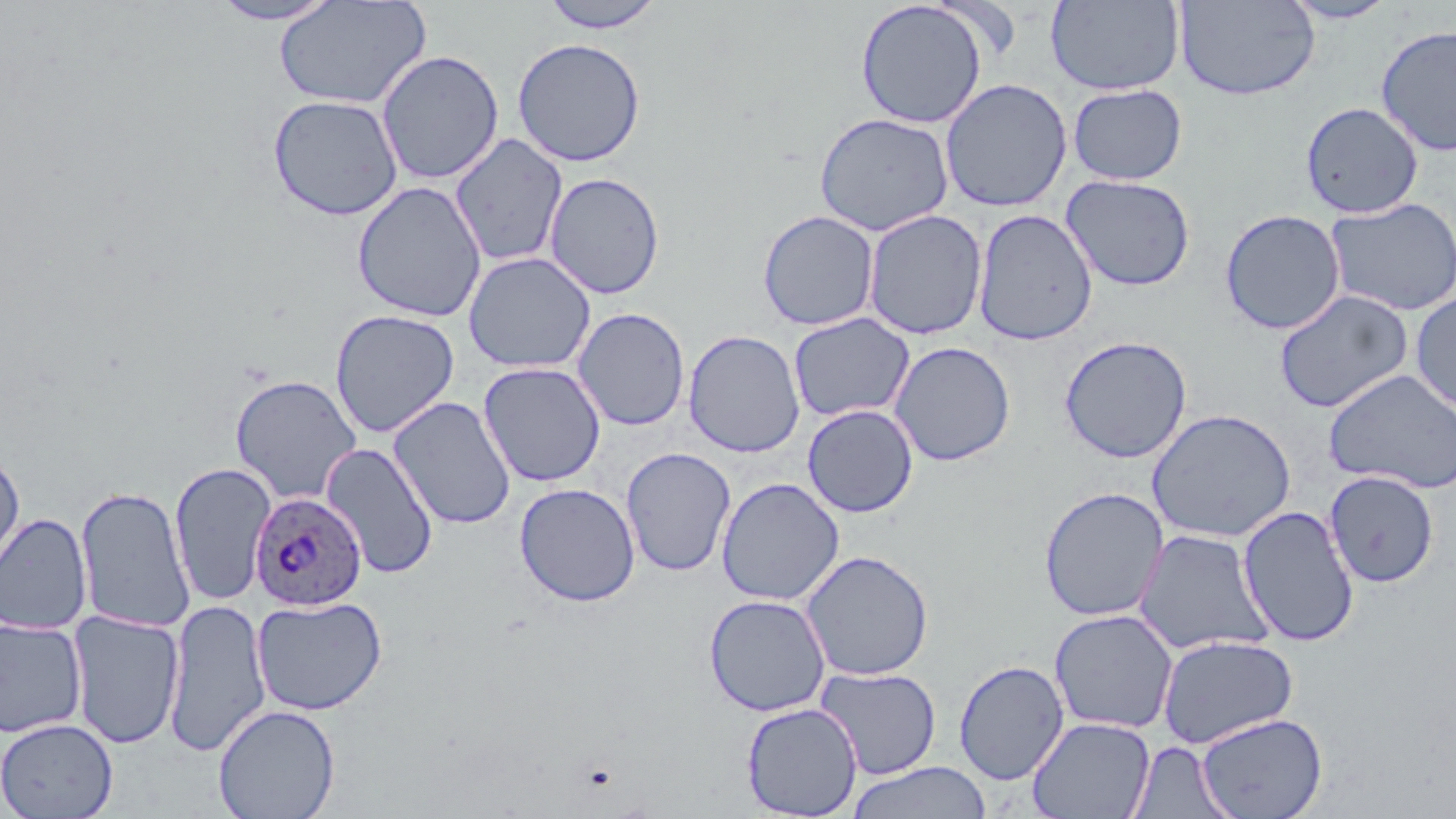
slide-level diagnosis = Plasmodium ovale
magnification = 1000x
Plasmodium ovale-infected red blood cell locations = approximate bounding boxes as named x1/y1/x2/y2 corners in pixels: (x1=249, y1=492, x2=366, y2=611)
modality = optical microscopy
field of view = one of a larger specimen
image size = 1456×819 pixels
uninfected red blood cell locations = approximate bounding boxes as named x1/y1/x2/y2 corners in pixels: (x1=207, y1=0, x2=343, y2=25), (x1=537, y1=0, x2=667, y2=33), (x1=1174, y1=0, x2=1320, y2=101), (x1=274, y1=1, x2=431, y2=110), (x1=855, y1=1, x2=988, y2=129), (x1=1046, y1=1, x2=1185, y2=95), (x1=1280, y1=1, x2=1399, y2=24), (x1=1375, y1=24, x2=1456, y2=158), (x1=511, y1=37, x2=646, y2=167), (x1=376, y1=49, x2=504, y2=185), (x1=939, y1=78, x2=1073, y2=212), (x1=1067, y1=84, x2=1188, y2=186), (x1=267, y1=94, x2=404, y2=221), (x1=1300, y1=101, x2=1423, y2=218), (x1=814, y1=112, x2=954, y2=236), (x1=449, y1=132, x2=568, y2=268), (x1=544, y1=171, x2=665, y2=300), (x1=1060, y1=174, x2=1196, y2=291), (x1=352, y1=181, x2=487, y2=322), (x1=1324, y1=197, x2=1456, y2=317), (x1=757, y1=209, x2=880, y2=331), (x1=862, y1=209, x2=988, y2=340), (x1=972, y1=209, x2=1098, y2=346), (x1=1220, y1=209, x2=1346, y2=335), (x1=463, y1=252, x2=596, y2=373), (x1=1274, y1=289, x2=1413, y2=413), (x1=1410, y1=292, x2=1456, y2=416), (x1=572, y1=307, x2=690, y2=431), (x1=329, y1=309, x2=460, y2=439), (x1=788, y1=312, x2=915, y2=423), (x1=683, y1=329, x2=805, y2=458), (x1=1058, y1=335, x2=1193, y2=464), (x1=889, y1=341, x2=1016, y2=466), (x1=478, y1=361, x2=606, y2=487), (x1=1324, y1=368, x2=1456, y2=494), (x1=230, y1=374, x2=362, y2=505), (x1=388, y1=395, x2=516, y2=530), (x1=802, y1=405, x2=918, y2=517), (x1=1146, y1=408, x2=1297, y2=543), (x1=320, y1=441, x2=439, y2=579), (x1=621, y1=447, x2=737, y2=577), (x1=0, y1=448, x2=25, y2=580), (x1=169, y1=461, x2=276, y2=606), (x1=1324, y1=471, x2=1439, y2=588), (x1=716, y1=477, x2=844, y2=606), (x1=514, y1=482, x2=641, y2=607), (x1=75, y1=484, x2=195, y2=633), (x1=1038, y1=486, x2=1169, y2=622), (x1=1238, y1=505, x2=1360, y2=647), (x1=0, y1=512, x2=92, y2=635), (x1=1134, y1=529, x2=1274, y2=656), (x1=801, y1=549, x2=934, y2=681), (x1=703, y1=594, x2=831, y2=717), (x1=251, y1=595, x2=387, y2=716), (x1=163, y1=598, x2=271, y2=757), (x1=1049, y1=609, x2=1178, y2=734), (x1=67, y1=610, x2=184, y2=749), (x1=0, y1=617, x2=87, y2=739), (x1=1156, y1=635, x2=1299, y2=749), (x1=953, y1=659, x2=1069, y2=785), (x1=816, y1=666, x2=942, y2=780), (x1=741, y1=702, x2=863, y2=818), (x1=213, y1=704, x2=340, y2=819), (x1=1195, y1=712, x2=1327, y2=819), (x1=1028, y1=716, x2=1155, y2=819), (x1=0, y1=718, x2=118, y2=819), (x1=1129, y1=741, x2=1235, y2=819), (x1=844, y1=761, x2=994, y2=819)
stain = May-Grünwald-Giemsa
preparation = thin blood film